Report the malaria status of this cell.
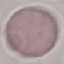

Uninfected.

Giemsa stain. Automatically extracted cell patch, resized to 64 × 64 pixels. Thin smear of blood. Acquired by smartphone through the microscope eyepiece.